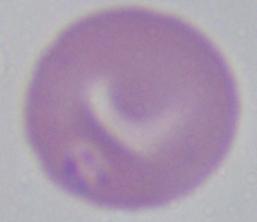

Summary:
  - Identification: Babesia
  - Modality: photomicrograph
  - Magnification: 1000x